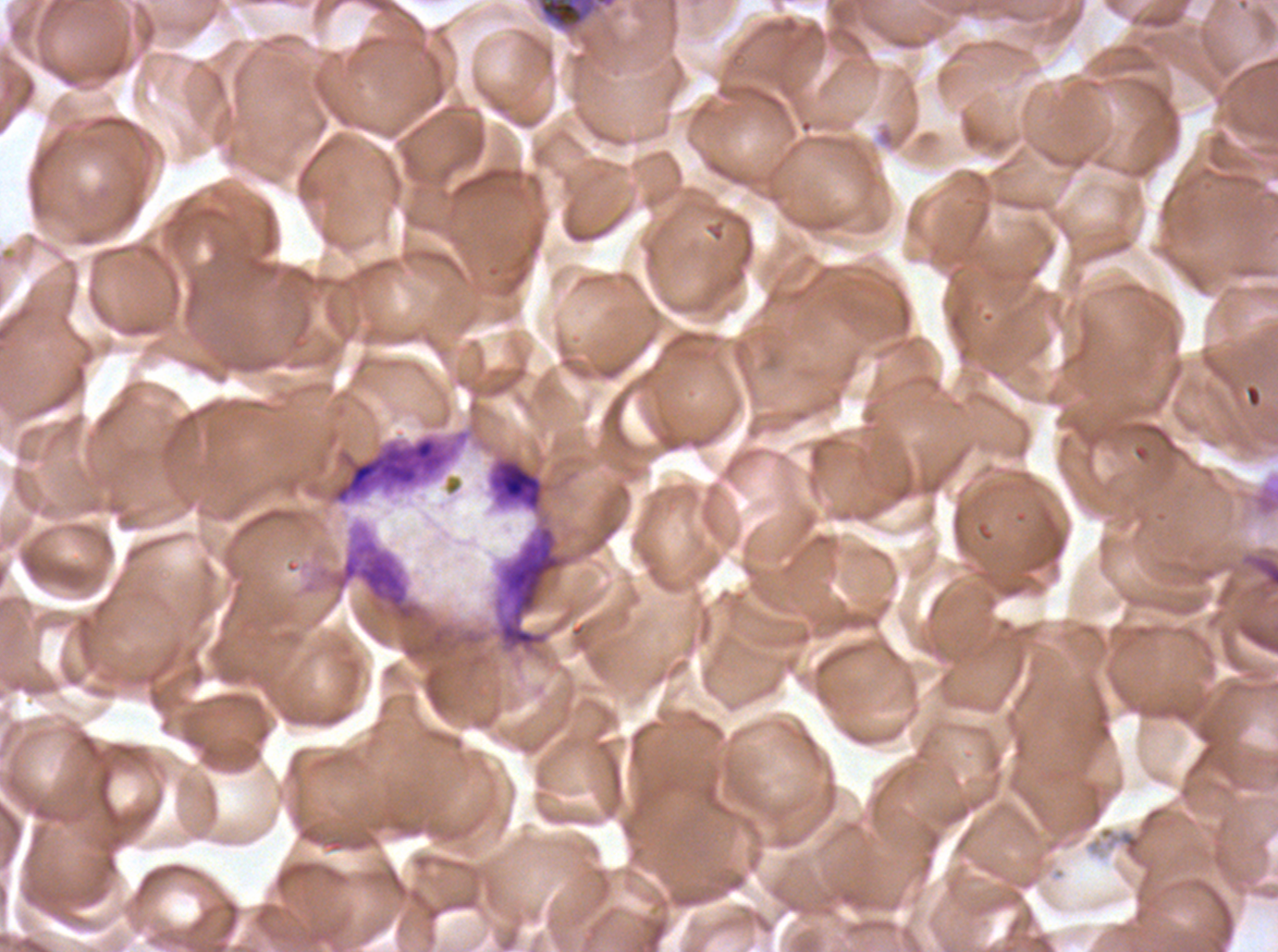

notation = approximate bounding boxes as [x1, y1, x2, y2] in pixels
debris locations = [327, 428, 472, 507]
early schizont locations = [535, 0, 617, 33]
image size = 1278×952 pixels
stain = Giemsa
specimen = ex-vivo P. falciparum culture from a patient in The Gambia, grown for 24 to 48 hours
preparation = thin blood smear
field of view = sub-image separated from a larger composite